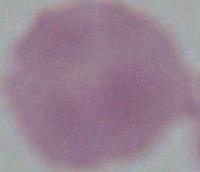 1000x magnification. A red blood cell is shown. Micrograph.